Classify this cell by malaria status.
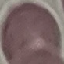

Uninfected.

stain = Giemsa
capture = smartphone camera at the microscope eyepiece
preparation = thin blood film
image type = automatically extracted cell patch, resized to 64 × 64 pixels